Locate every malaria parasite and every leukocyte.
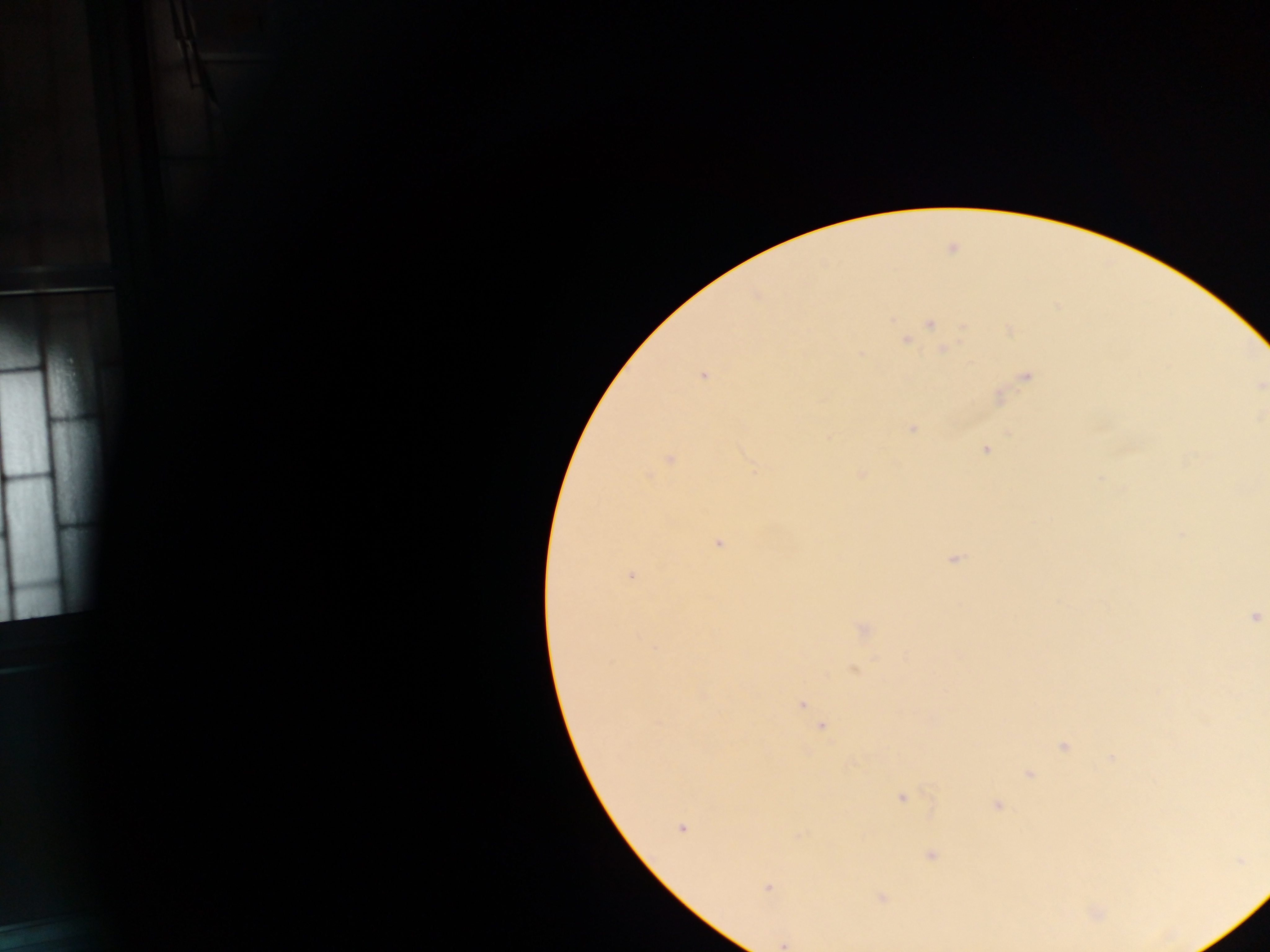

Approximate centers as {x, y} in pixels.
Malaria parasites: {930, 324}, {703, 375}, {912, 426}, {986, 450}, {718, 543}, {633, 574}, {1255, 616}, {802, 705}, {820, 727}, {901, 798}, {681, 830}, {931, 854}.
No leukocytes observed.

Collected in Ghana. Thick blood smear. Image is 1270×952 pixels. One field of view. Mobile-phone photograph taken through the microscope.